Give the position of every leukocyte visible.
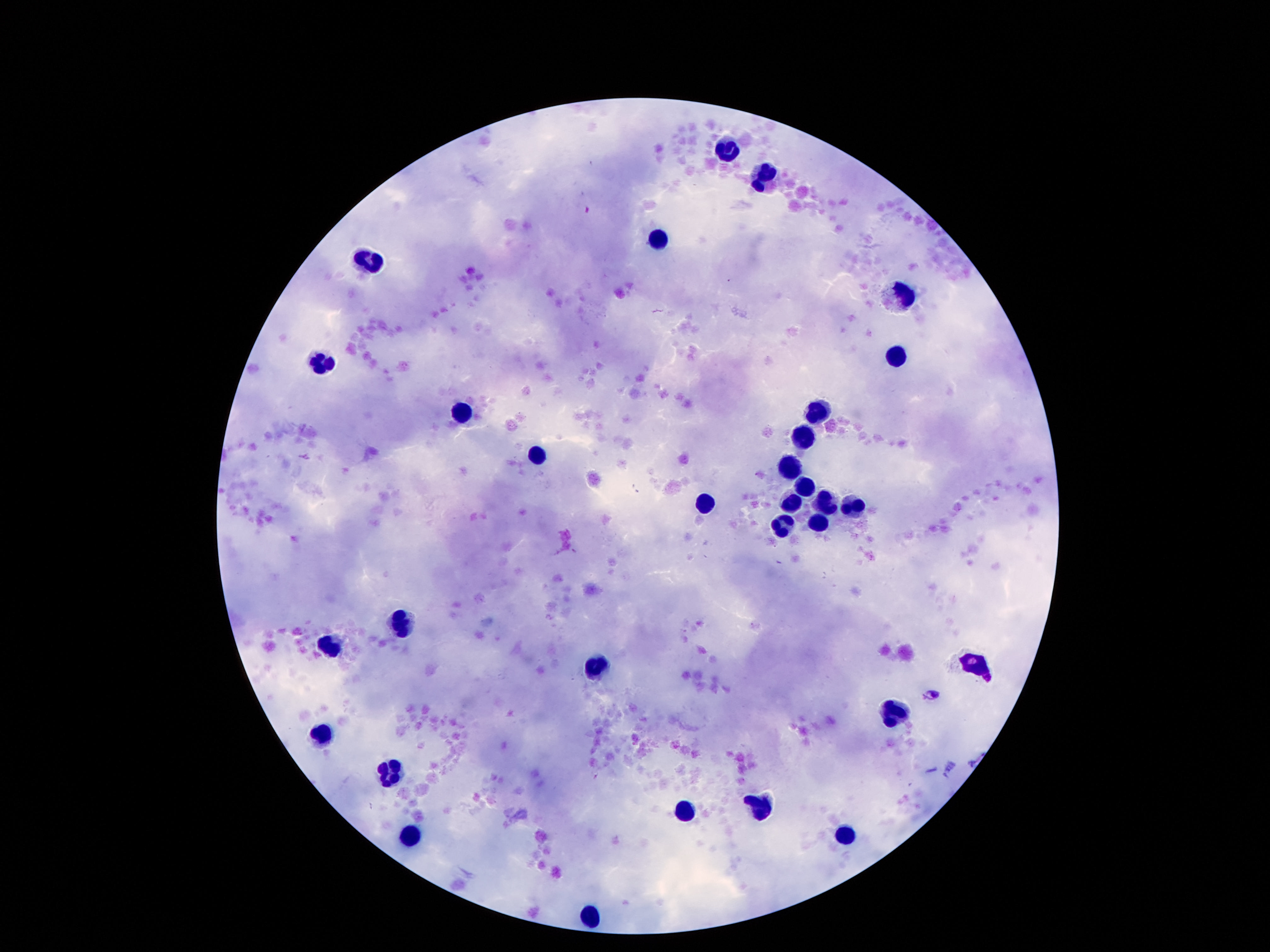
Approximate centers as (x, y) in pixels.
Leukocytes: (727, 151), (769, 179), (657, 242), (370, 256), (900, 293), (895, 356), (321, 361), (820, 408), (463, 412), (801, 438), (538, 456), (790, 466), (801, 489), (703, 501), (792, 501), (827, 505), (848, 510), (820, 524), (783, 526), (400, 622), (328, 648), (596, 664), (972, 664), (897, 711), (323, 730), (395, 779), (759, 804), (685, 811), (844, 835), (416, 839), (591, 909).

100x magnification. Image is 1270×952 pixels. Patient malaria status: negative. Thick blood film. Giemsa-stained preparation. Smartphone photograph taken through the microscope eyepiece. Single field of view.